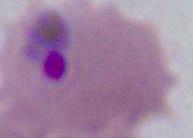
A Plasmodium parasite is shown. Micrograph. Captured at either 400x or 1000x magnification.